Assess the background quality.
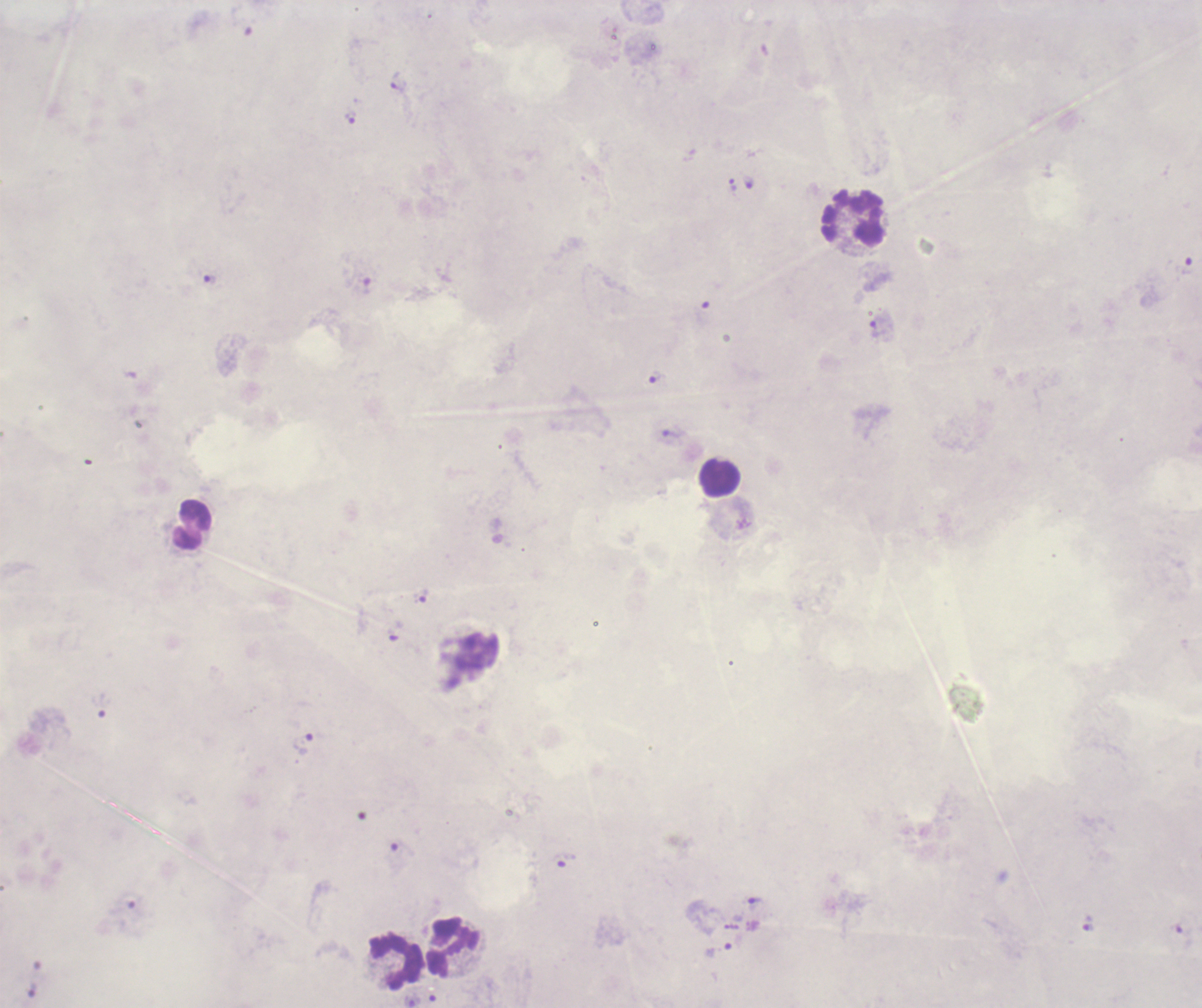
It is poor.

coordinate format = approximate centers as (x, y) in pixels
leukocyte locations = (854, 219), (720, 477), (192, 525), (455, 946), (395, 961)
trophozoite locations = (399, 83), (352, 119), (750, 184), (210, 280), (881, 329), (656, 378), (672, 433), (419, 594), (302, 742), (566, 860), (757, 903), (1089, 925), (718, 951)
result = malaria parasites detected
image size = 1202×1008 pixels
coloration quality = bad
magnification = 100x
preparation = thick blood film
field of view = one from this slide
stain = Romanowsky
context = previously used in a real diagnosis